Outline each Plasmodium vivax-infected red blood cell.
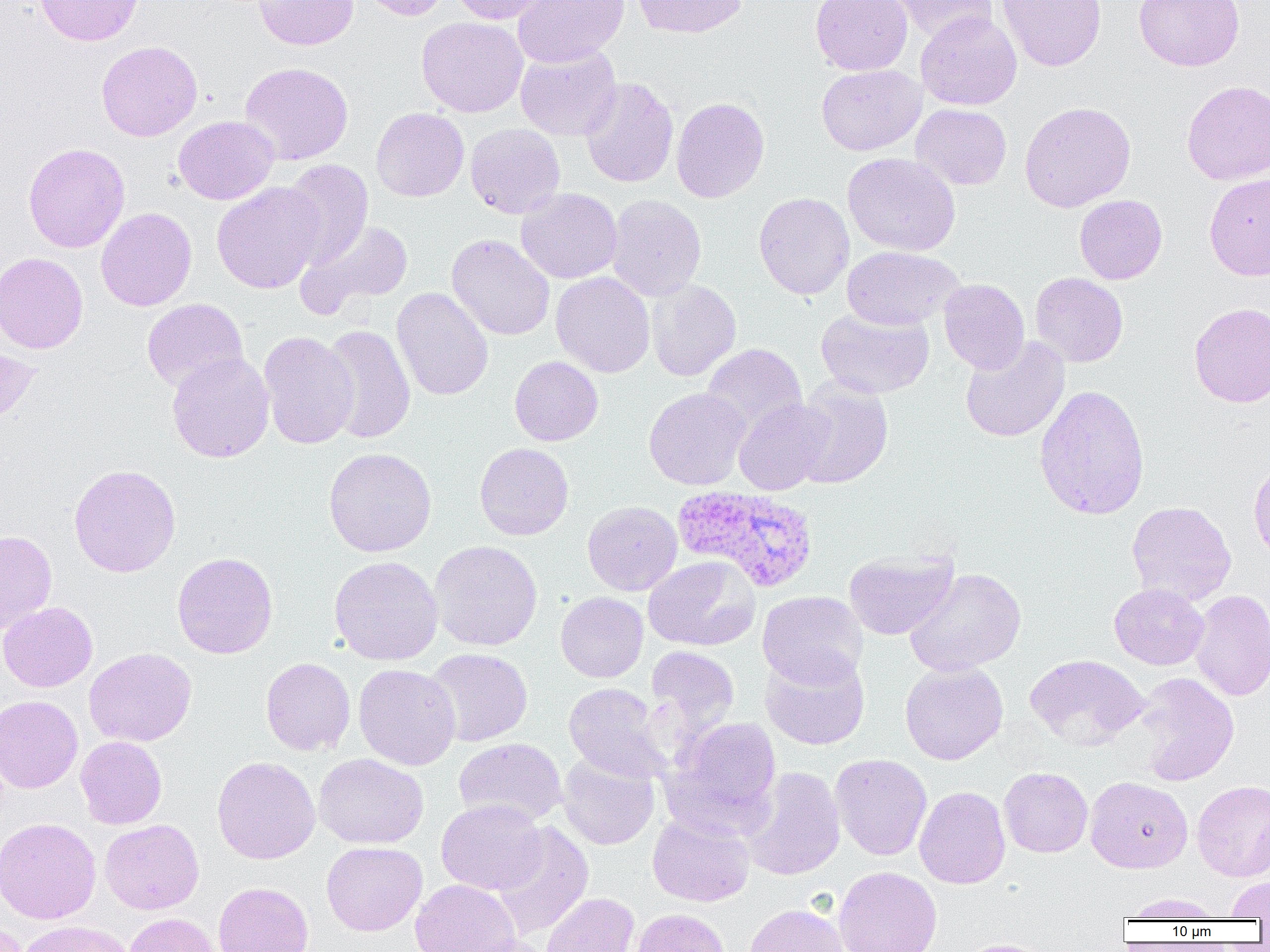

Approximate bounding boxes as [x1, y1, x2, y2] in pixels.
Plasmodium vivax-infected red blood cells: [672, 484, 819, 593].

Uninfected red blood cell locations: [35, 0, 144, 46], [254, 0, 358, 50], [358, 0, 452, 20], [449, 0, 553, 24], [512, 0, 629, 67], [632, 0, 748, 38], [810, 0, 912, 75], [888, 0, 997, 44], [997, 0, 1107, 71], [1134, 0, 1244, 71], [915, 12, 1022, 110], [417, 16, 528, 117], [97, 40, 202, 141], [515, 45, 622, 141], [240, 62, 353, 165], [816, 64, 925, 155], [580, 77, 679, 188], [1182, 81, 1270, 184], [671, 97, 770, 203], [1019, 101, 1136, 212], [911, 103, 1012, 190], [371, 107, 469, 201], [173, 116, 278, 204], [465, 123, 566, 219], [23, 143, 130, 253], [843, 152, 961, 256], [281, 159, 373, 268], [1203, 173, 1270, 281], [212, 182, 324, 294], [516, 188, 622, 283], [753, 192, 854, 299], [606, 194, 707, 301], [1074, 194, 1167, 284], [96, 207, 197, 311], [298, 218, 414, 315], [447, 233, 555, 341], [842, 246, 963, 330], [0, 252, 88, 354], [551, 272, 655, 377], [1029, 272, 1128, 367], [646, 279, 741, 381], [939, 279, 1029, 374], [392, 287, 493, 401], [141, 298, 247, 392], [1189, 301, 1270, 408], [815, 306, 935, 399], [320, 324, 416, 444], [258, 331, 358, 449], [960, 337, 1070, 442], [702, 343, 807, 435], [0, 344, 40, 424], [167, 352, 275, 463], [509, 356, 603, 446], [791, 378, 893, 489], [1034, 384, 1151, 520], [644, 387, 751, 490], [733, 397, 834, 495], [474, 442, 574, 541], [323, 447, 437, 557], [1248, 459, 1270, 564], [68, 464, 181, 577], [582, 501, 682, 596], [1126, 501, 1236, 606], [0, 530, 57, 635], [429, 540, 543, 651], [844, 548, 959, 641], [172, 552, 278, 658], [329, 555, 443, 665], [345, 555, 450, 769], [644, 556, 759, 651], [904, 567, 1026, 676], [1109, 583, 1209, 670], [1190, 589, 1270, 701], [757, 591, 868, 688], [555, 592, 648, 682], [0, 601, 97, 692], [645, 645, 740, 739], [84, 647, 197, 746], [424, 648, 533, 746], [760, 649, 870, 750], [1025, 653, 1148, 750], [261, 657, 356, 756], [900, 661, 1008, 765], [354, 663, 461, 770], [1131, 672, 1240, 786], [563, 683, 669, 782], [0, 695, 83, 793], [665, 717, 782, 831], [75, 736, 167, 829], [453, 738, 567, 827], [556, 752, 660, 850], [313, 753, 428, 849], [830, 753, 932, 861], [212, 756, 321, 864], [741, 766, 846, 880], [999, 767, 1093, 858], [1085, 776, 1193, 873], [1192, 779, 1270, 881], [914, 786, 1010, 889], [436, 799, 547, 894], [647, 812, 755, 907], [0, 817, 101, 924], [100, 819, 204, 914], [491, 822, 594, 940], [322, 841, 427, 935], [833, 866, 942, 952], [1225, 876, 1270, 918], [411, 879, 521, 952], [213, 881, 313, 952], [540, 892, 640, 952], [1122, 893, 1225, 920], [744, 903, 850, 952], [631, 908, 730, 952], [123, 913, 222, 952], [0, 919, 28, 952], [15, 920, 135, 952], [457, 935, 556, 952], [957, 938, 1057, 952]. Slide-level diagnosis: Plasmodium vivax. Thin blood smear. Captured at 1000x magnification. Light microscopy. One field of a larger specimen. Image is 1270×952 pixels.